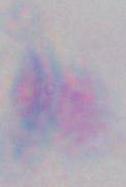

{
  "modality": "photomicrograph",
  "identification": "Toxoplasma gondii",
  "magnification": "1000x"
}